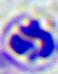

Summary:
  - Magnification: 400x
  - Modality: photomicrograph
  - Identification: white blood cell